Give the position of every Plasmodium parasite.
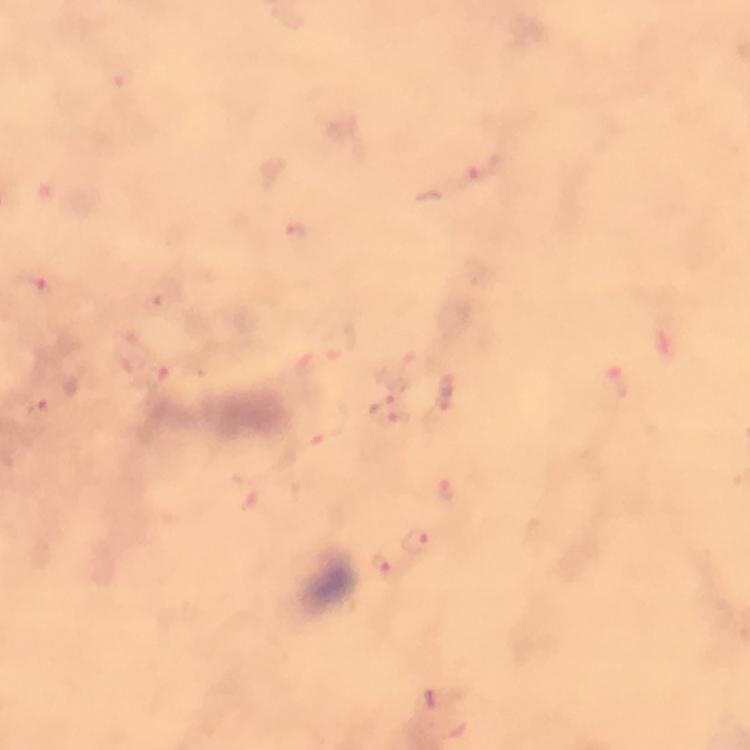

Approximate centers as {x, y} in pixels.
Plasmodium parasites: {474, 173}, {296, 234}, {28, 287}, {340, 341}, {153, 377}, {618, 383}, {445, 394}, {380, 405}, {42, 415}, {400, 422}, {329, 423}, {447, 488}.

Summary:
  - Preparation: thick blood smear
  - Context: from a diagnostic examination for malaria
  - Cropped from: a single field of view
  - Stain: Giemsa
  - Immersion oil: used
  - Magnification: 100x
  - Image size: 750×750 pixels
  - Capture: smartphone mounted on the microscope